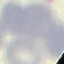

Malaria status: uninfected. Thin blood smear. Giemsa stain. Acquired by smartphone through the microscope eyepiece. Automatically extracted cell patch, resized to 64 × 64 pixels.